Locate every blood parasite and identify its species.
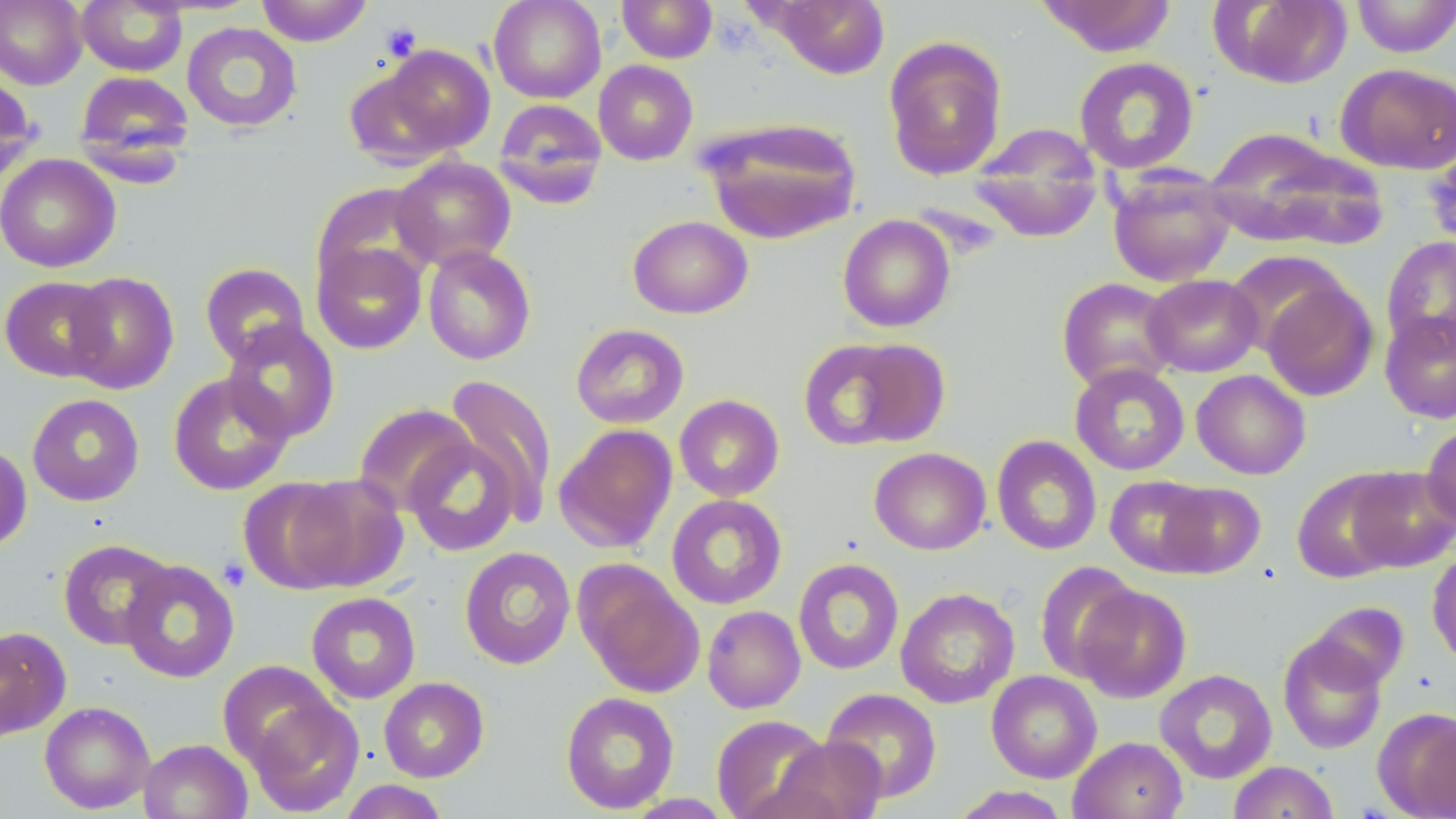

No blood parasites observed.

Approximate bounding boxes as (x1, y1, x2, y2) in pixels. Platelet locations: (381, 23, 421, 61), (217, 558, 250, 592). Uninfected red blood cell locations: (0, 0, 87, 89), (256, 0, 373, 46), (488, 0, 606, 103), (617, 0, 718, 63), (768, 0, 891, 79), (1036, 0, 1179, 56), (1213, 0, 1352, 89), (1351, 0, 1456, 58), (77, 1, 188, 76), (181, 21, 302, 132), (883, 36, 1008, 181), (370, 44, 496, 158), (1074, 56, 1199, 173), (593, 60, 698, 165), (1335, 62, 1456, 175), (74, 70, 195, 170), (0, 71, 38, 184), (492, 97, 608, 207), (700, 116, 862, 245), (968, 125, 1104, 242), (1204, 127, 1366, 248), (0, 153, 121, 273), (391, 156, 516, 270), (1107, 166, 1236, 287), (312, 181, 439, 292), (837, 214, 956, 333), (628, 215, 752, 318), (1381, 236, 1456, 355), (312, 241, 427, 354), (423, 245, 536, 365), (1224, 251, 1349, 357), (200, 262, 311, 367), (64, 270, 179, 394), (1142, 274, 1263, 377), (0, 276, 115, 382), (1260, 276, 1379, 401), (1056, 277, 1179, 392), (1380, 308, 1456, 423), (221, 321, 340, 442), (570, 323, 689, 429), (797, 336, 943, 451), (1070, 363, 1190, 475), (1191, 369, 1311, 480), (168, 372, 294, 495), (444, 373, 558, 524), (27, 393, 145, 506), (674, 394, 785, 502), (354, 402, 476, 515), (554, 423, 677, 553), (1421, 424, 1456, 529), (404, 434, 522, 557), (991, 434, 1103, 556), (0, 442, 32, 554), (869, 447, 991, 555), (1345, 466, 1456, 571), (1292, 469, 1411, 583), (280, 473, 409, 592), (1104, 475, 1218, 576), (1154, 481, 1265, 578), (666, 493, 787, 609), (58, 539, 174, 650), (459, 546, 576, 670), (1427, 549, 1456, 668), (793, 557, 904, 675), (120, 559, 240, 683), (574, 560, 704, 699), (1034, 561, 1142, 683), (1074, 584, 1191, 703), (895, 587, 1019, 708), (305, 591, 421, 704), (1305, 601, 1410, 693), (702, 605, 805, 713), (0, 626, 70, 740), (1278, 633, 1388, 754), (216, 659, 340, 769), (1155, 669, 1277, 784), (986, 670, 1102, 783), (379, 677, 489, 782), (821, 687, 942, 803), (560, 691, 680, 814), (245, 694, 364, 816), (39, 700, 155, 814), (1374, 706, 1456, 818), (711, 715, 831, 819), (1068, 736, 1188, 819), (772, 737, 885, 818), (138, 738, 252, 819), (1228, 760, 1339, 819), (339, 779, 452, 818), (949, 785, 1071, 818), (623, 794, 735, 819). Slide-level diagnosis: no evidence of blood parasites. Image is 1456×819 pixels. Optical microscopy. May-Grünwald-Giemsa-stained preparation. Captured at 1000x magnification. One field of a larger specimen. Thin blood film.